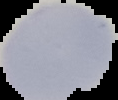

image type = cell region segmented out of the field of view; surrounding area masked to black
result = no Plasmodium parasites seen
preparation = thin blood smear
image size = 118×100 pixels